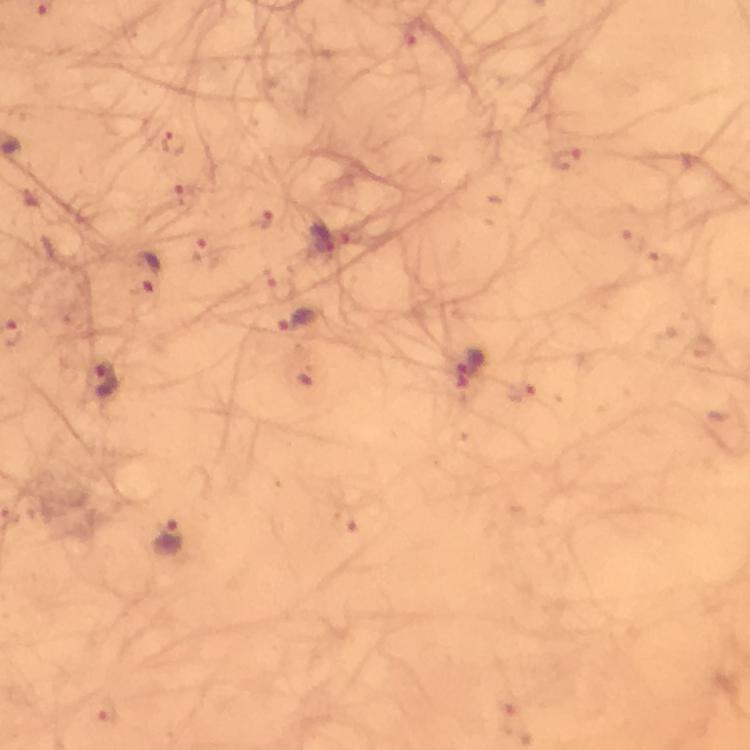
capture = smartphone mounted on the microscope
stain = Giemsa
context = from a diagnostic examination for malaria
image size = 750×750 pixels
immersion oil = applied
magnification = 100x
malaria parasite locations = approximate centers as {x, y} in pixels: {175, 142}, {323, 238}, {147, 276}, {302, 321}, {471, 370}, {106, 379}, {170, 539}
preparation = thick blood film
cropped from = a single field of view